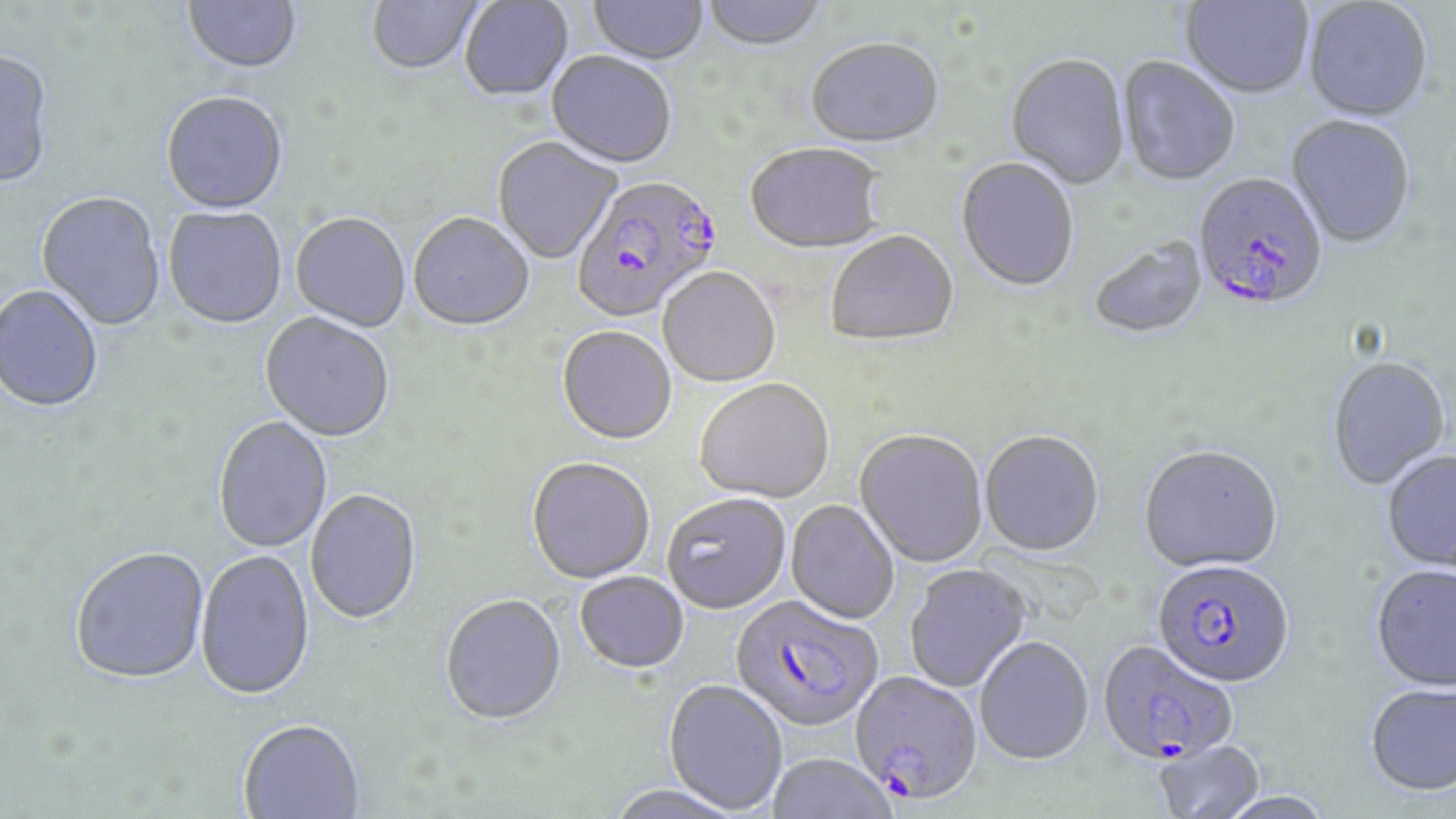

Approximate bounding boxes as (x1,y1)-(x2,y2) corner pairs in pixels. Uninfected red blood cell locations: (182,0)-(302,77), (367,0)-(483,77), (588,0)-(707,67), (701,0)-(830,53), (460,1)-(574,103), (1180,1)-(1313,101), (1304,1)-(1432,124), (806,41)-(944,150), (0,53)-(55,190), (547,54)-(677,170), (1005,56)-(1131,191), (1116,58)-(1241,189), (161,93)-(288,216), (1286,117)-(1416,251), (492,138)-(621,265), (744,144)-(884,257), (956,159)-(1079,294), (36,194)-(165,332), (163,207)-(287,330), (290,214)-(410,334), (409,215)-(534,334), (826,233)-(959,349), (1089,239)-(1208,341), (658,269)-(780,389), (0,287)-(103,414), (259,314)-(395,444), (557,328)-(677,447), (1327,357)-(1452,490), (695,381)-(834,505), (213,417)-(332,554), (854,431)-(987,569), (979,432)-(1104,559), (1139,448)-(1282,575), (1382,452)-(1456,573), (526,459)-(655,585), (305,491)-(422,626), (661,495)-(791,616), (785,501)-(899,625), (71,549)-(209,687), (194,551)-(315,703), (1370,564)-(1456,692), (905,566)-(1031,693), (575,574)-(689,675), (440,597)-(567,728), (975,639)-(1094,767), (662,680)-(788,815), (1365,683)-(1456,796), (239,722)-(364,819), (1153,739)-(1265,819), (767,754)-(896,819), (604,785)-(746,819). Plasmodium falciparum-infected red blood cell locations: (1193,173)-(1330,315), (572,177)-(725,326), (1151,560)-(1295,691), (730,596)-(884,735), (1097,640)-(1239,766), (848,672)-(983,809). Slide-level diagnosis: Plasmodium falciparum. Captured at 1000x magnification. Image is 1456×819 pixels. Thin blood smear. May-Grünwald-Giemsa stain. Single field of view. Optical microscopy.